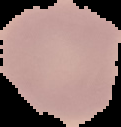

Image is 121×127 pixels. Malaria status: uninfected. From a thin blood film. The area outside the segmented cell region is set to black.